Locate every malaria parasite.
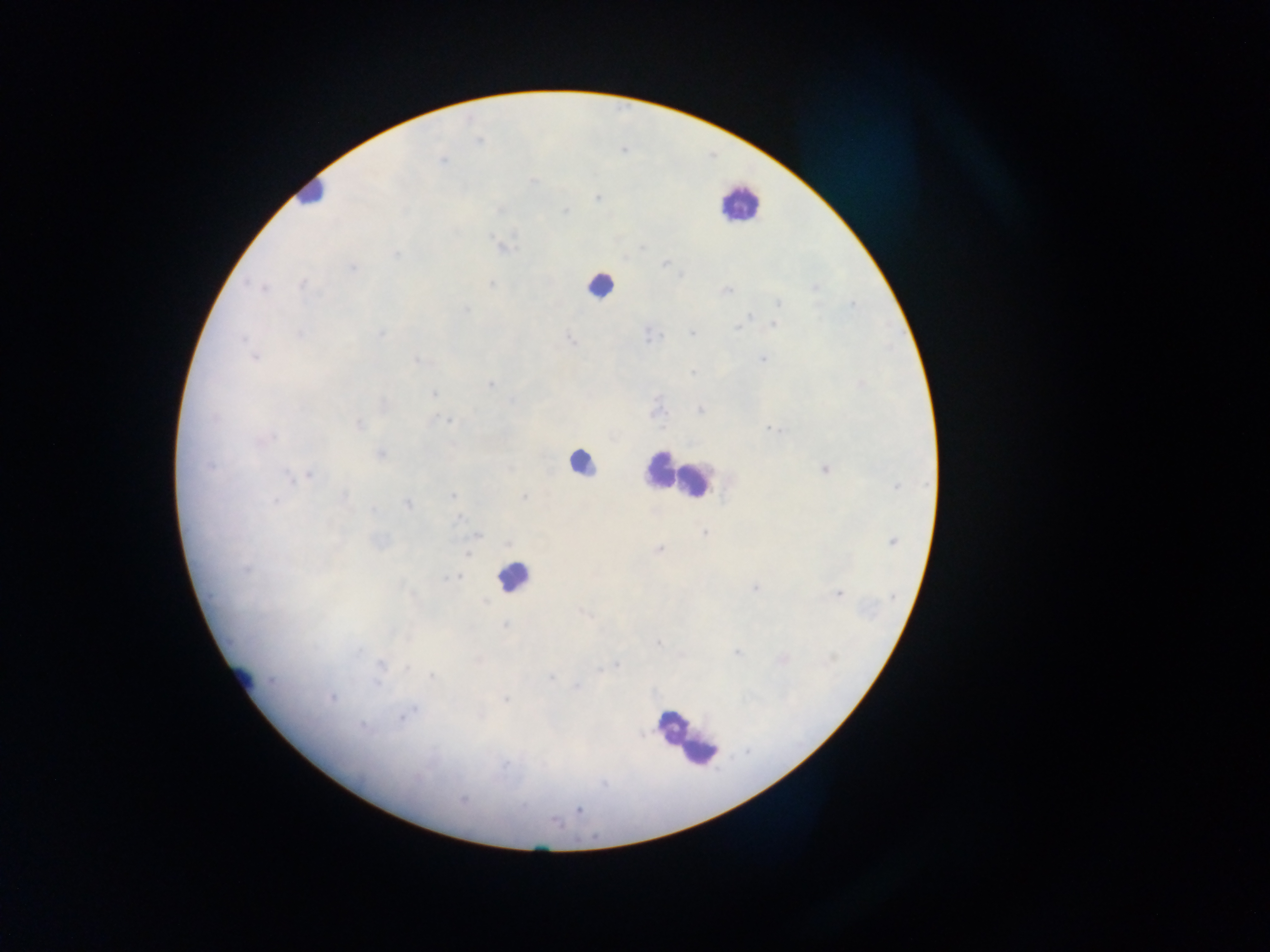
Approximate centers as x y in pixels.
Malaria parasites: 443 160; 533 181; 597 198; 565 211; 503 247; 642 247; 396 255; 665 264; 353 268; 681 276; 301 284; 491 285; 815 286; 263 288; 726 291; 779 303; 852 305; 466 309; 750 317; 744 322; 774 325; 739 327; 300 334; 381 334; 692 334; 649 336; 243 338; 570 340; 255 357; 762 359; 417 361; 692 372; 490 383; 434 394; 512 400; 701 410; 657 412; 447 420; 360 424; 772 429; 272 437; 381 454; 825 469; 310 475; 290 478; 896 487; 453 495; 345 497; 524 497; 276 500; 408 504; 373 509; 458 519; 705 532; 478 536; 893 541; 659 549; 467 554; 247 571; 453 578; 755 589; 838 594; 892 597; 485 602; 582 612; 505 625; 658 642; 359 651; 737 653; 381 664; 615 665; 408 668; 599 670; 431 675; 551 677; 377 683; 577 687; 332 698; 506 699; 414 709; 401 718; 364 727; 640 734; 417 777; 603 783; 462 800; 579 810.

preparation = thick blood smear
field of view = single
country = Ghana
leukocyte locations = approximate centers as x y in pixels: 308 193; 739 203; 599 285; 581 460; 659 470; 695 482; 513 577; 239 674; 672 723; 682 737; 701 751
image size = 1270×952 pixels
capture = mobile-phone photograph through a microscope